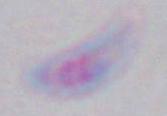
modality = photomicrograph
identification = Toxoplasma gondii
magnification = 1000x